Assess this cell for malaria.
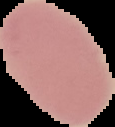
It is uninfected.

Summary:
  - Preparation: thin blood film
  - Image size: 115×127 pixels
  - Image type: cell region segmented out of the field of view; surrounding area masked to black